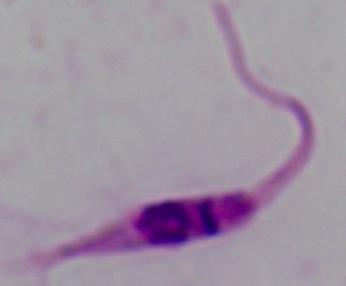 Photomicrograph. Captured at 1000x magnification. A Leishmania parasite is shown.